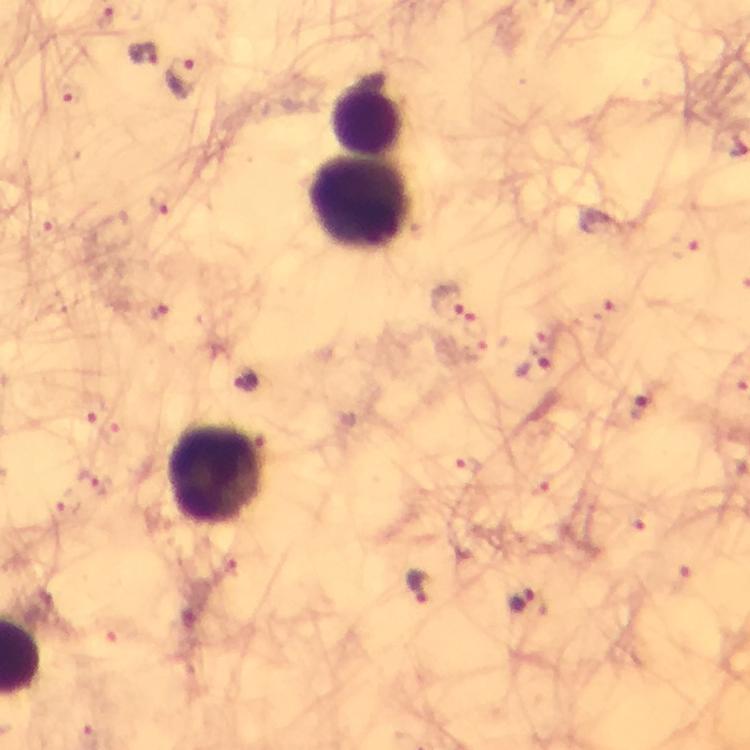
Approximate object centers, in pixels from the top-left corner. Malaria parasite locations: (x=144, y=54), (x=180, y=77), (x=70, y=98), (x=161, y=200), (x=48, y=226), (x=684, y=246), (x=445, y=301), (x=158, y=311), (x=609, y=313), (x=543, y=341), (x=476, y=347), (x=643, y=406), (x=91, y=408), (x=468, y=463), (x=94, y=480), (x=540, y=483), (x=68, y=504), (x=636, y=518), (x=680, y=580), (x=414, y=587), (x=522, y=600), (x=121, y=632). Leukocyte locations: (x=370, y=112), (x=361, y=203), (x=217, y=476). 100x magnification. Giemsa-stained preparation. A crop from one field of view. Image is 750×750 pixels. Thick blood film. From a diagnostic examination for malaria. Photographed through the microscope with a smartphone camera. Immersion oil applied.